Outline each uninfected red blood cell.
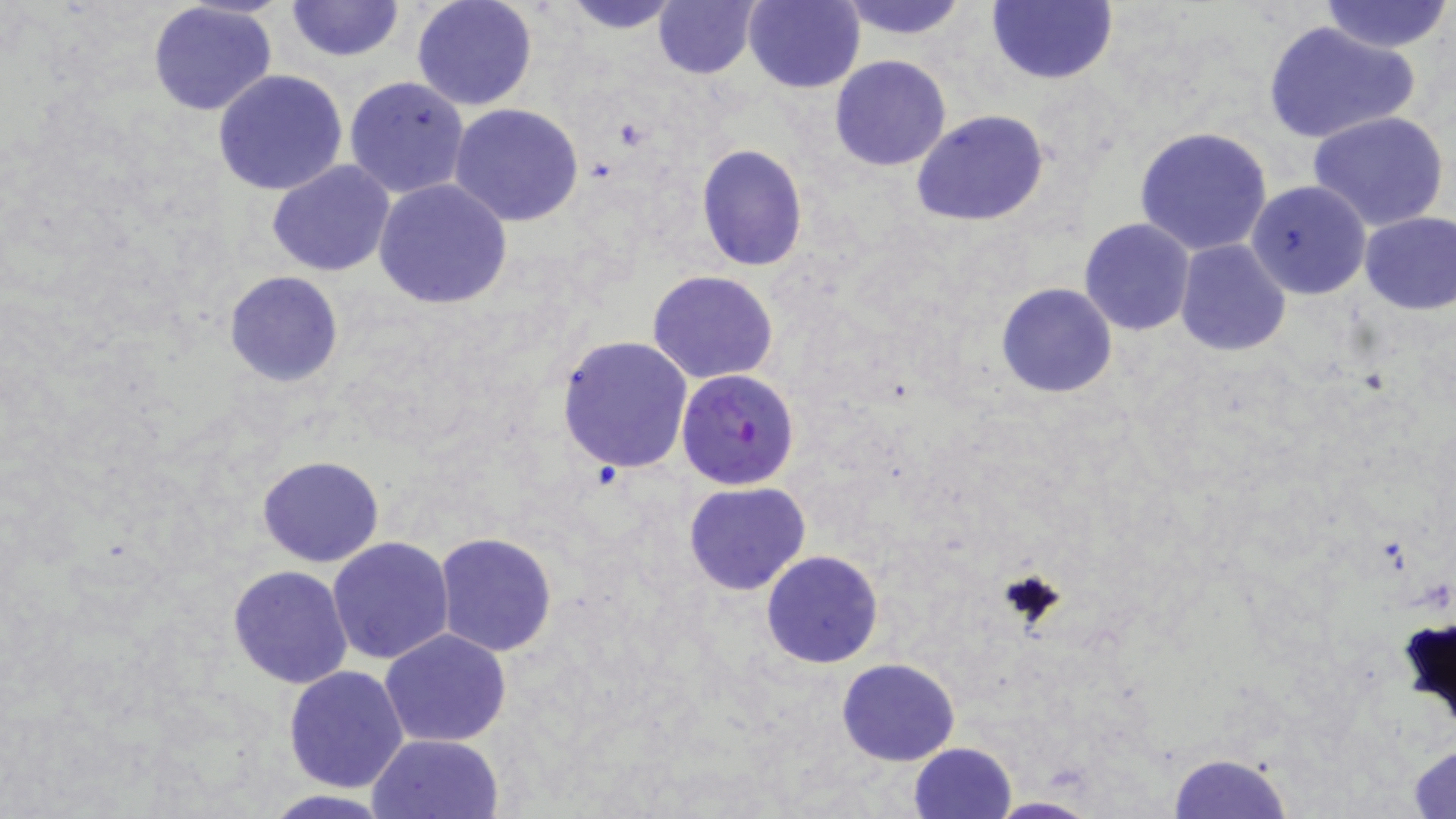
Approximate bounding boxes as [x1, y1, x2, y2] in pixels.
Uninfected red blood cells: [286, 0, 402, 62], [557, 0, 686, 33], [743, 0, 865, 93], [835, 0, 971, 41], [986, 0, 1116, 85], [147, 1, 277, 116], [411, 1, 538, 112], [653, 1, 761, 79], [1318, 1, 1452, 53], [1262, 19, 1418, 148], [829, 55, 953, 171], [212, 68, 349, 195], [343, 75, 472, 199], [450, 105, 585, 226], [912, 110, 1050, 228], [1306, 111, 1451, 235], [1133, 125, 1273, 257], [696, 144, 807, 271], [268, 160, 396, 277], [373, 179, 514, 308], [1246, 179, 1372, 300], [1359, 211, 1456, 313], [1079, 219, 1196, 336], [1174, 238, 1290, 356], [649, 270, 779, 385], [222, 272, 343, 387], [996, 282, 1118, 398], [557, 334, 694, 473], [256, 456, 385, 569], [684, 481, 811, 596], [433, 533, 558, 658], [328, 537, 457, 665], [761, 549, 883, 668], [227, 564, 354, 688], [1398, 608, 1456, 738], [379, 629, 512, 748], [837, 657, 960, 766], [283, 664, 411, 793], [366, 733, 503, 818], [908, 741, 1017, 819], [1409, 742, 1456, 817], [1166, 750, 1293, 818], [255, 790, 401, 818], [987, 796, 1099, 818].

plasmodium_falciparum_infected_red_blood_cell_locations: 'approximate bounding boxes as [x1, y1, x2, y2] in pixels: [676, 369, 801, 491]'
slide_level_diagnosis: Plasmodium falciparum
magnification: 1000x
modality: optical microscopy
image_size: 1456×819 pixels
field_of_view: single
preparation: thin blood smear
stain: May-Grünwald-Giemsa